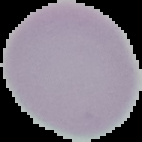

From a thin blood film. Image is 142×142 pixels. Result: no Plasmodium parasites seen. The area outside the segmented cell region is set to black.